Report the malaria status of this cell.
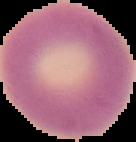

It is uninfected.

preparation = thin blood film
image type = cell region segmented out of the field of view; surrounding area masked to black
image size = 136×142 pixels